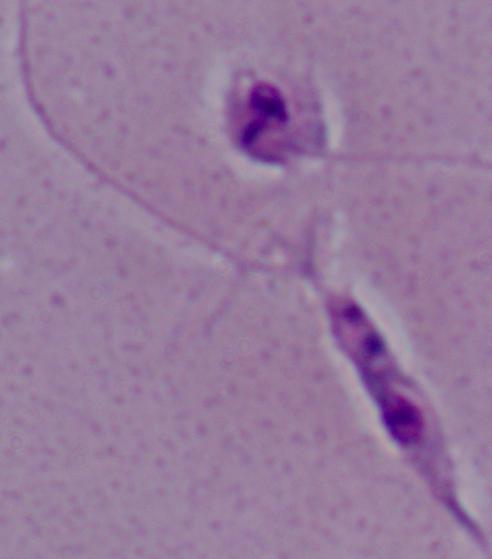

Captured at 1000x magnification. A Leishmania parasite is seen. Photomicrograph.